Give the extent of all Plasmodium falciparum-infected red blood cells.
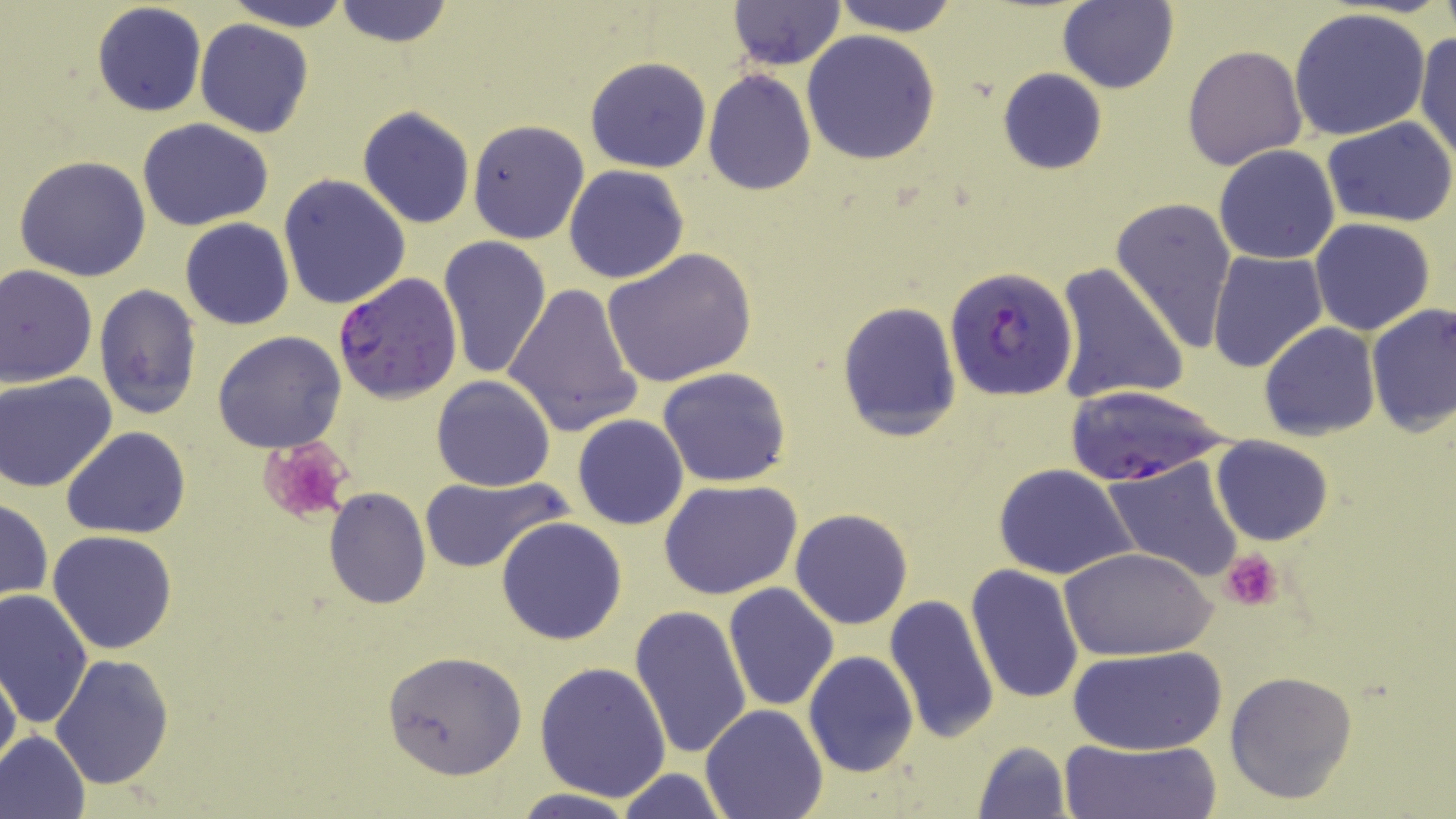

Approximate bounding boxes as (x1,y1)-(x2,y2) corner pairs in pixels.
Plasmodium falciparum-infected red blood cells: (944,265)-(1077,400), (332,274)-(463,401), (1061,385)-(1233,488).

Summary:
  - Platelet locations: (257,436)-(353,526), (1222,550)-(1281,611)
  - Uninfected red blood cell locations: (221,0)-(357,30), (832,0)-(961,36), (727,1)-(845,69), (92,2)-(207,117), (332,2)-(456,49), (1059,2)-(1178,94), (1289,8)-(1432,142), (194,20)-(315,138), (1413,30)-(1456,165), (802,31)-(941,164), (1182,45)-(1306,169), (585,56)-(711,173), (997,68)-(1108,176), (703,70)-(816,194), (356,106)-(476,229), (1324,117)-(1456,226), (136,118)-(275,233), (466,119)-(590,245), (1213,144)-(1340,265), (13,155)-(152,281), (563,164)-(690,284), (278,173)-(411,310), (1111,196)-(1237,351), (1310,217)-(1436,336), (180,218)-(295,330), (439,236)-(553,380), (602,248)-(756,387), (1207,249)-(1328,372), (0,263)-(99,387), (1053,263)-(1189,406), (503,282)-(642,438), (93,284)-(203,420), (836,298)-(963,441), (1365,300)-(1455,439), (1258,323)-(1380,441), (212,330)-(347,454), (658,366)-(792,488), (1,372)-(119,493), (432,375)-(557,491), (572,414)-(689,530), (62,426)-(190,539), (1211,436)-(1334,546), (1102,457)-(1244,583), (992,463)-(1138,581), (417,473)-(570,572), (658,479)-(802,600), (1070,484)-(1223,631), (323,489)-(430,609), (679,489)-(819,685), (1,497)-(51,605), (789,508)-(913,630), (496,517)-(627,646), (46,529)-(178,655), (1063,547)-(1215,660), (965,564)-(1085,706), (723,583)-(839,712), (0,589)-(95,729), (883,595)-(1001,743), (629,604)-(754,762), (1066,646)-(1227,755), (381,649)-(529,780), (803,651)-(919,777), (49,652)-(175,791), (0,659)-(20,775), (535,661)-(672,801), (1225,671)-(1358,804), (700,703)-(828,819), (0,730)-(91,819), (1059,737)-(1221,818), (970,740)-(1074,819), (614,768)-(730,819), (511,789)-(636,818)
  - Slide-level diagnosis: Plasmodium falciparum
  - Modality: light microscopy
  - Stain: May-Grünwald-Giemsa
  - Preparation: thin blood smear
  - Field of view: single
  - Magnification: 1000x
  - Image size: 1456×819 pixels